Classify this cell by malaria status.
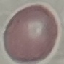

It is uninfected.

Giemsa stain. Thin blood smear. Cell patch, automatically extracted from a larger field of view and resized to 64 × 64 pixels. Photographed with a smartphone camera at the microscope eyepiece.